Describe the morphology of the erythrocytes.
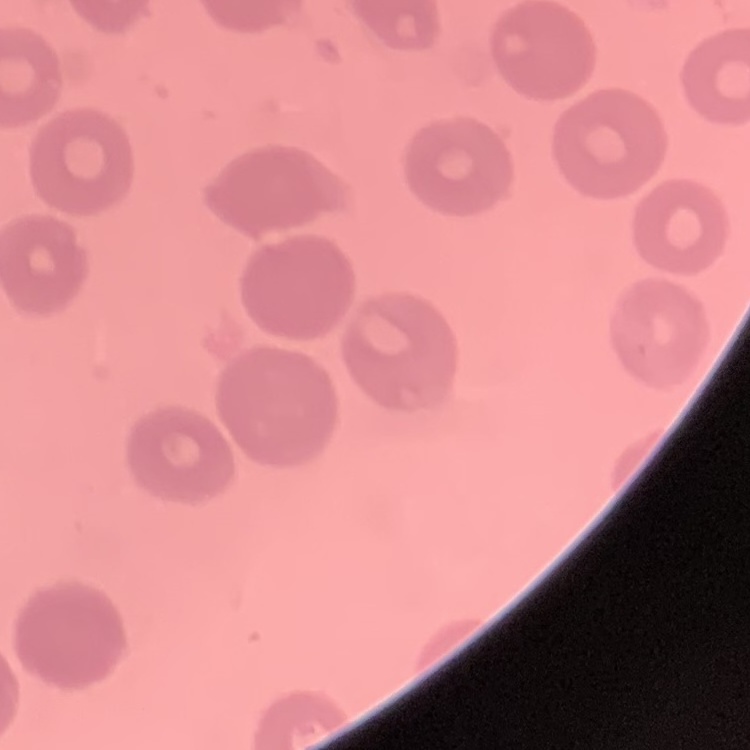

They show no rouleaux formation.

stain: Field's or Giemsa
preparation: thin blood smear
image_type: one tile cut from a larger photomicrograph